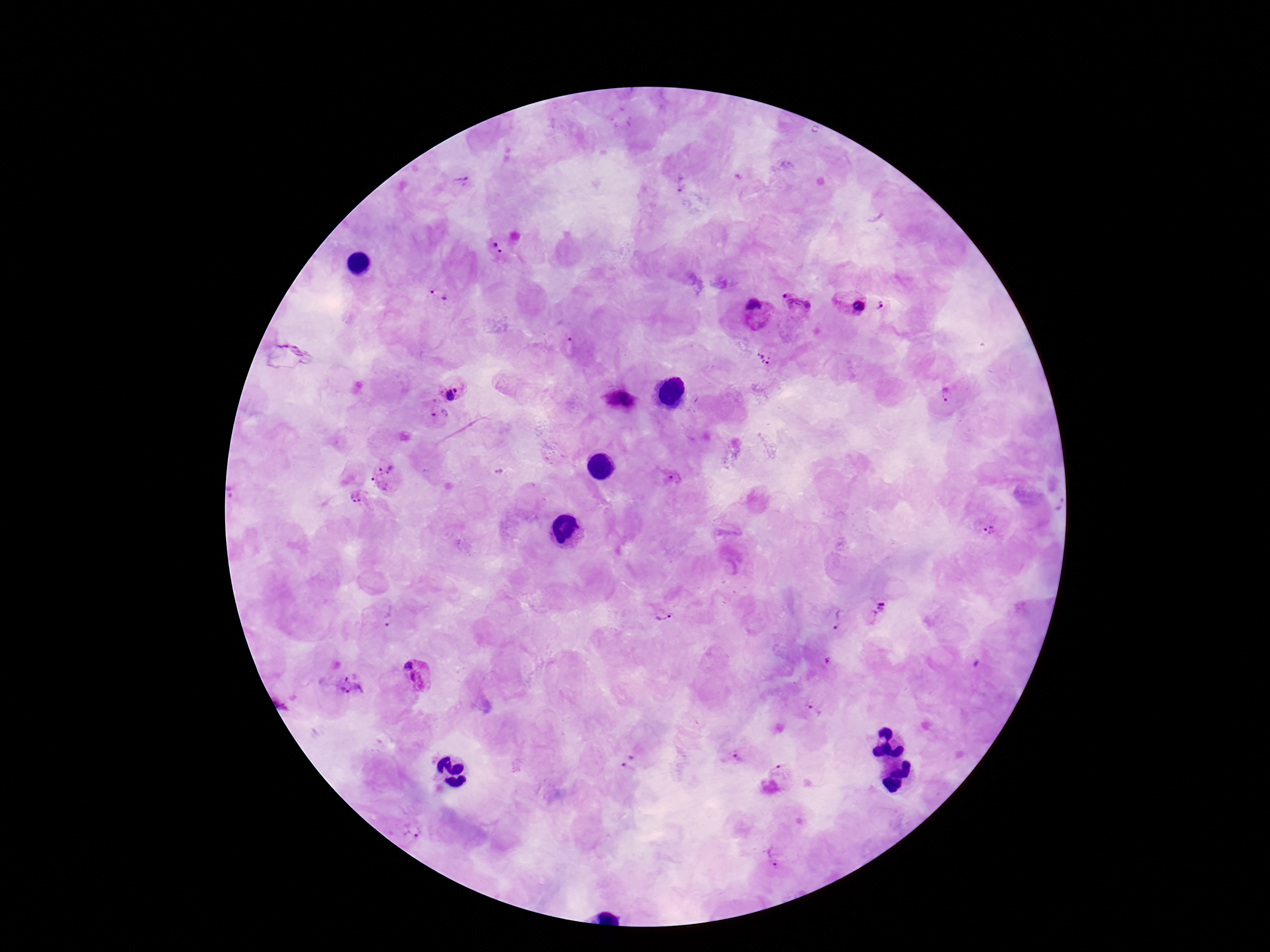 Approximate object centers, in pixels from the top-left corner. Plasmodium parasite locations: (x=465, y=183), (x=681, y=186), (x=500, y=246), (x=437, y=296), (x=850, y=300), (x=797, y=303), (x=881, y=305), (x=757, y=311), (x=765, y=359), (x=451, y=388), (x=947, y=396), (x=621, y=400), (x=429, y=417), (x=384, y=476), (x=674, y=479), (x=352, y=502), (x=988, y=530), (x=663, y=611), (x=876, y=612), (x=387, y=616), (x=836, y=620), (x=417, y=675), (x=350, y=685), (x=815, y=711), (x=736, y=758), (x=630, y=762), (x=783, y=771), (x=412, y=830), (x=774, y=858). Image is 1270×952 pixels. Patient malaria status: infected. Thick blood smear. Giemsa stain. 100x magnification. Smartphone photograph taken through the microscope eyepiece. Single field of view.